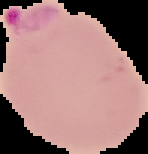

image type = segmented cell region on a black background
preparation = thin blood film
image size = 148×154 pixels
result = malaria parasites detected